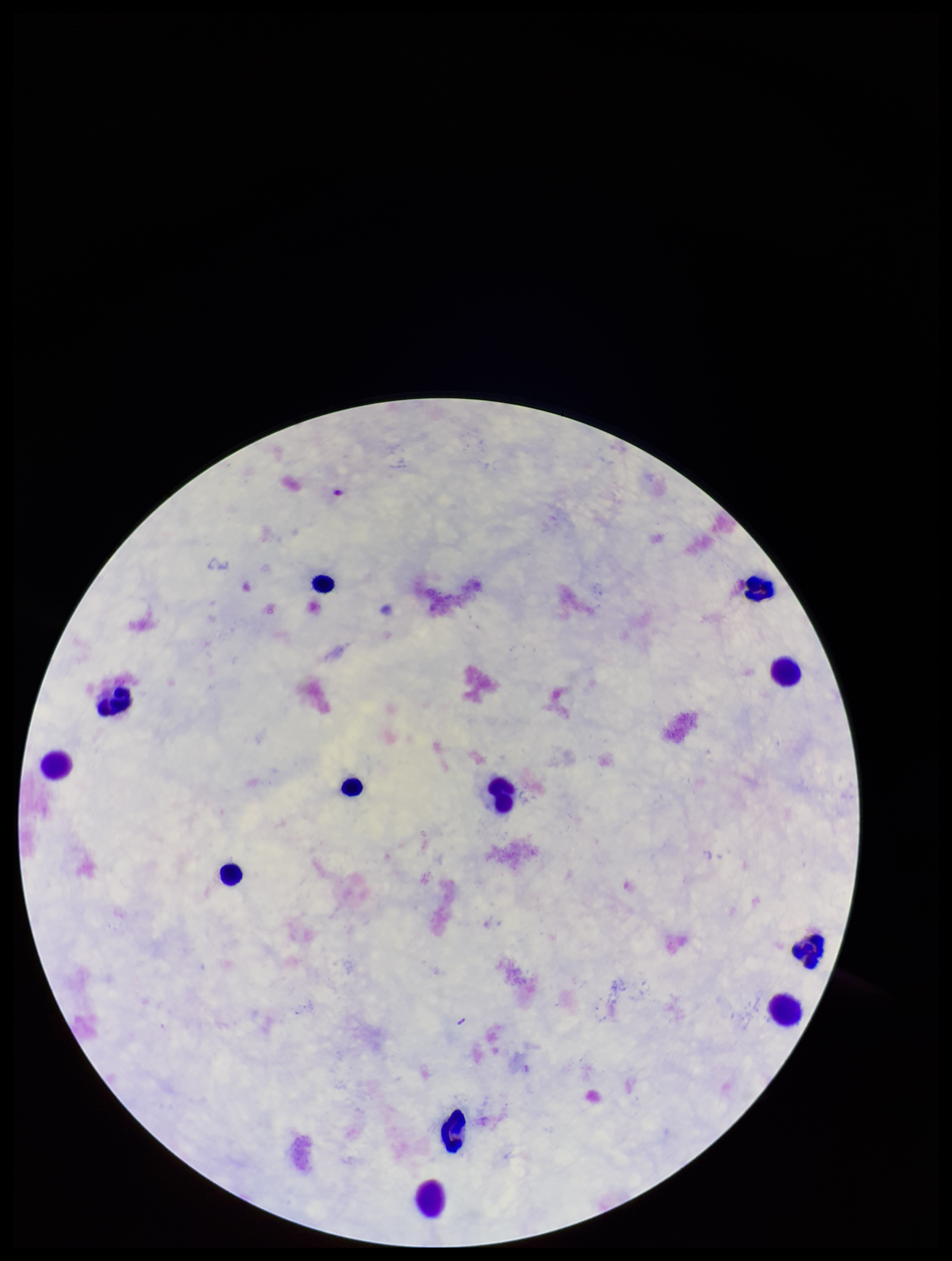 Patient malaria status: negative. Preparation: thick. Image is 952×1261 pixels. Photographed through the microscope eyepiece with a smartphone camera. Leukocyte count: 12. One field from this slide. Parasite count: 0. Stained with Giemsa. Plasmodium parasites: none detected.